Report the malaria status of this cell.
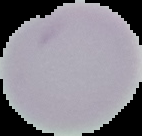

It is uninfected.

Image is 142×136 pixels. From a thin blood film. Segmented cell region on a black background.